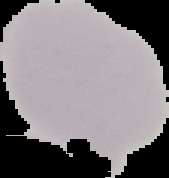
image_size: 169×178 pixels
image_type: segmented cell region with the area outside set to black
preparation: thin blood film
result: no malaria parasites seen